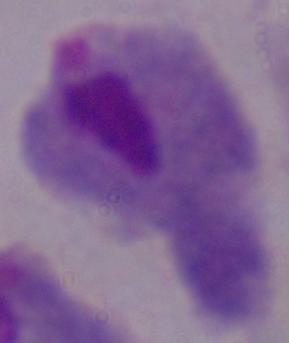

Summary:
  - Magnification: 1000x
  - Modality: photomicrograph
  - Identification: trichomonad